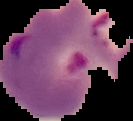
Cell region segmented out of the field of view; the surrounding area is masked to black. Image is 133×121 pixels. Result: malaria parasites identified. From a thin blood film.